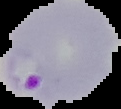

Summary:
  - Result: malaria parasites identified
  - Preparation: thin blood smear
  - Image type: segmented cell region on a black background
  - Image size: 121×109 pixels